Classify this cell by malaria status.
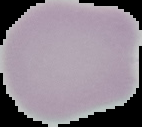
It is uninfected.

image size = 142×127 pixels
preparation = thin blood smear
image type = segmented cell region with the area outside set to black